Report the malaria status of this cell.
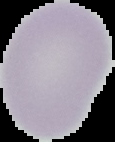

Uninfected.

Summary:
  - Image size: 115×142 pixels
  - Preparation: thin blood film
  - Image type: segmented cell region on a black background